Assess this cell for malaria.
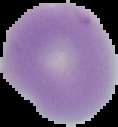
Uninfected.

image type = segmented cell region with the area outside set to black
preparation = thin blood smear
image size = 118×127 pixels